Report the malaria status of this cell.
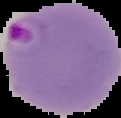

It is parasitized.

image type = segmented cell region with the area outside set to black
image size = 121×118 pixels
preparation = thin blood smear